Identify the preparation type.
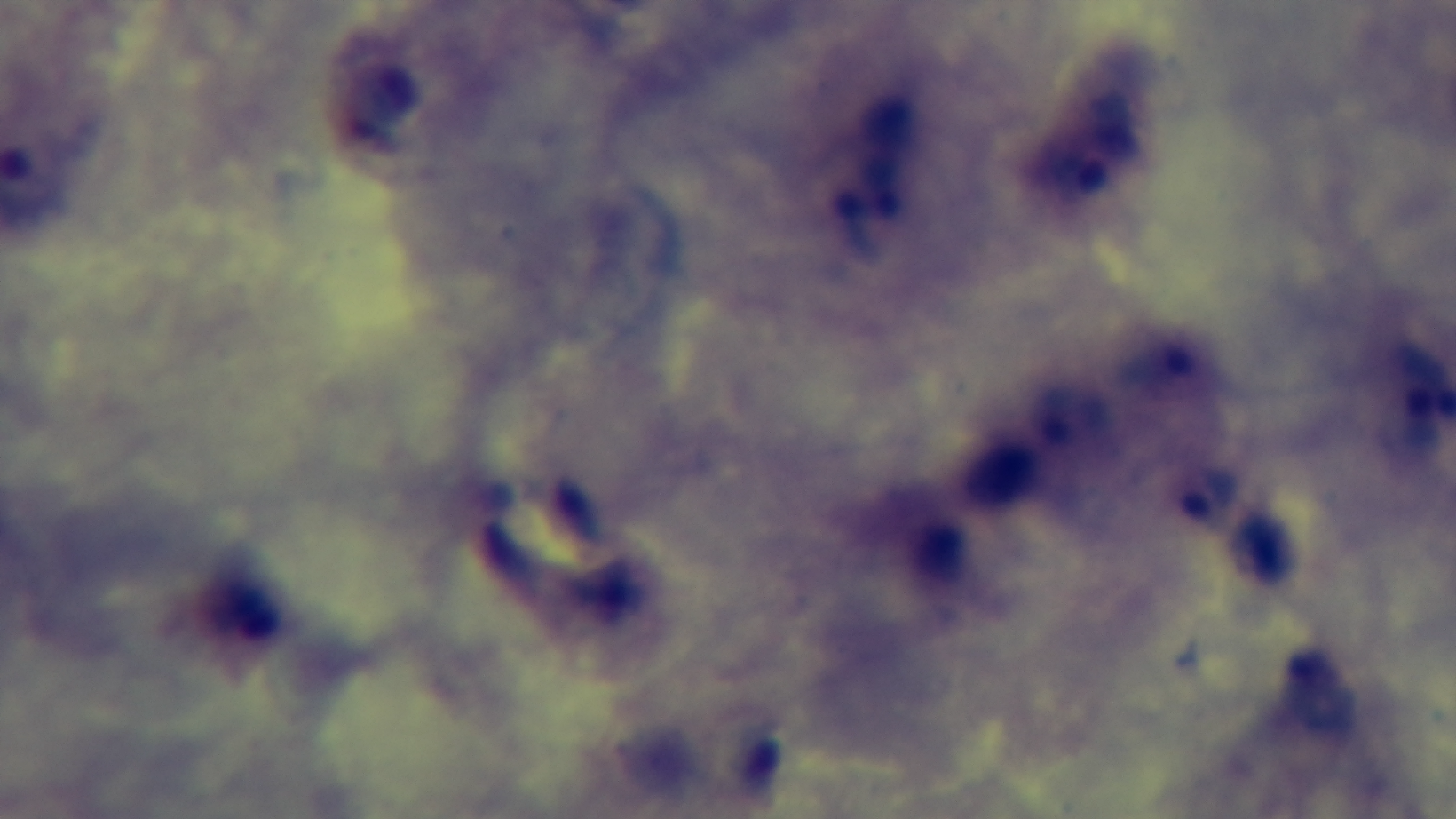

A thick smear.

Summary:
  - Stain: Giemsa
  - Objective: 100x oil immersion
  - Modality: light microscopy
  - Field of view: one from the slide
  - Malaria status: infected
  - Capture: mounted 4K digital camera